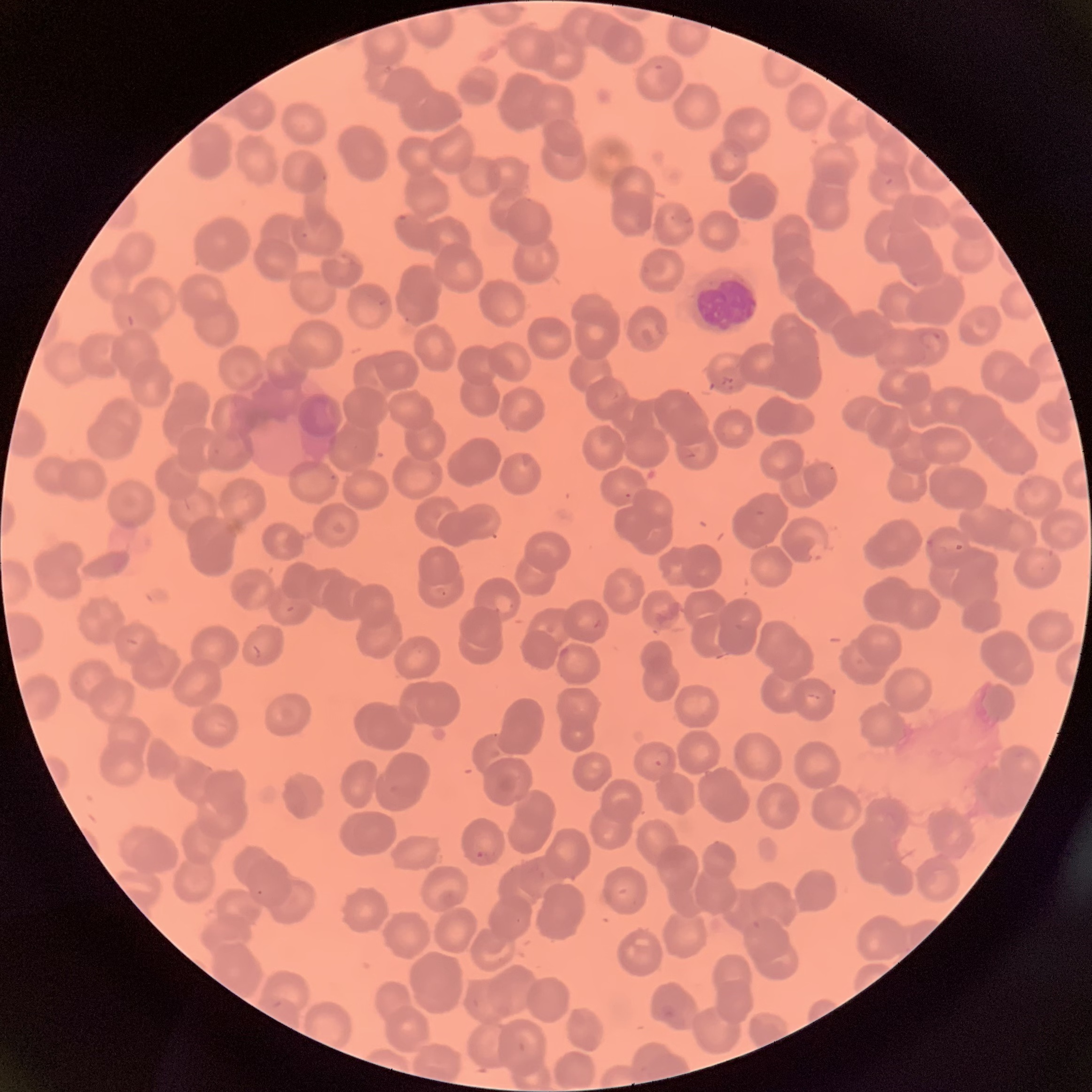 Approximate bounding boxes as named x1/y1/x2/y2 corners in pixels. White blood cell locations: (x1=692, y1=269, x2=760, y2=333). Plasmodium parasite locations: (x1=918, y1=329, x2=944, y2=352), (x1=719, y1=375, x2=737, y2=391), (x1=925, y1=539, x2=934, y2=545), (x1=808, y1=543, x2=828, y2=562), (x1=436, y1=586, x2=446, y2=596), (x1=653, y1=749, x2=672, y2=768), (x1=475, y1=851, x2=494, y2=860), (x1=659, y1=1003, x2=677, y2=1021). The red blood cells show rouleaux formation. Thin blood smear. Image is 1092×1092 pixels. Optical microscopy.